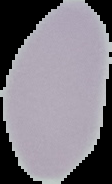

image size = 112×184 pixels
image type = cell region segmented out of the field of view; surrounding area masked to black
preparation = thin blood film
malaria status = uninfected